Assess this cell for malaria.
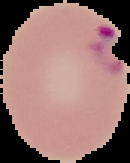

It is parasitized.

image_size: 130×163 pixels
image_type: cell region segmented out of the field of view; surrounding area masked to black
preparation: thin blood smear